Outline each Plasmodium ovale-infected red blood cell.
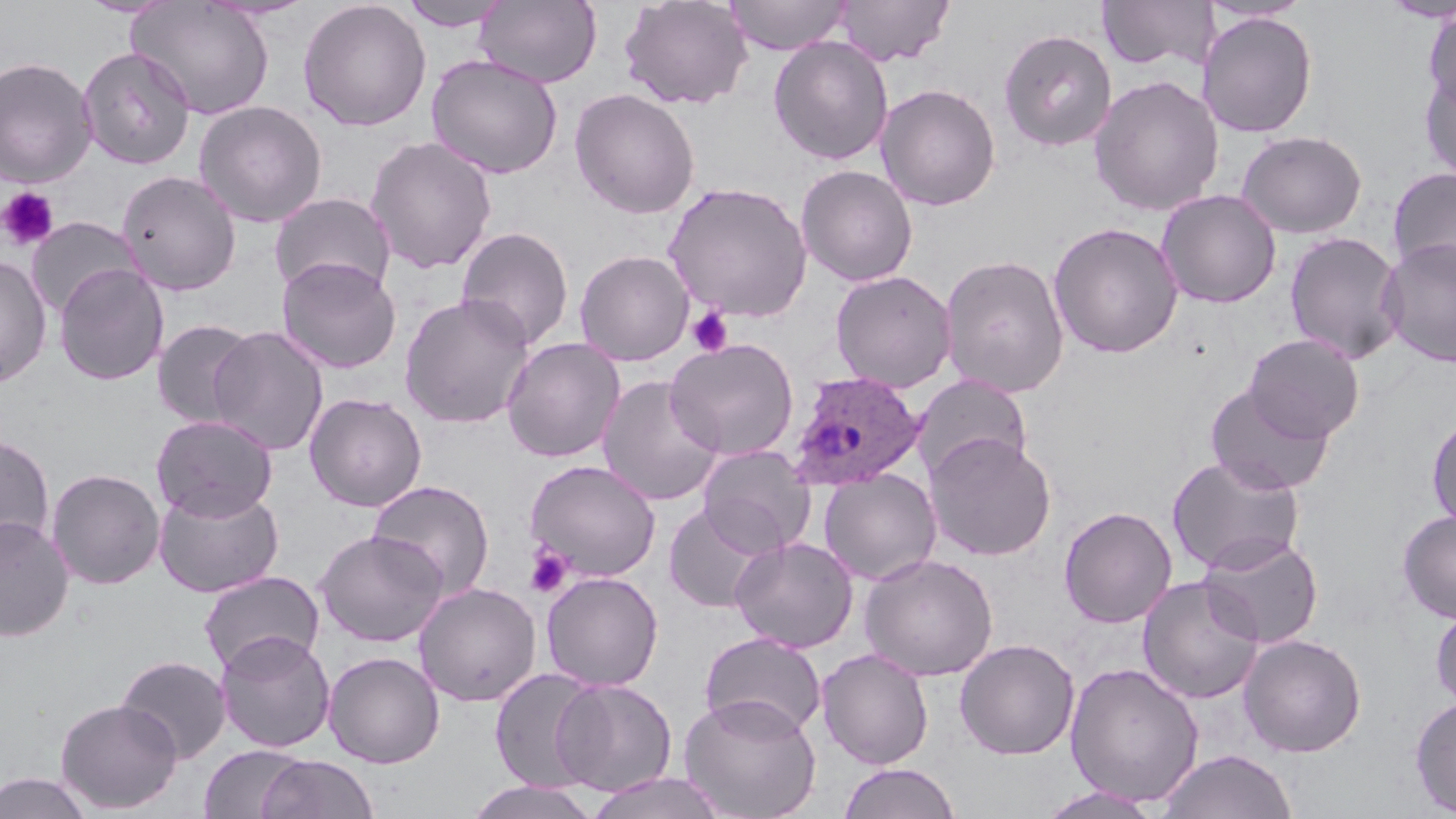

Approximate bounding boxes as (x1, y1, x2, y2) in pixels.
Plasmodium ovale-infected red blood cells: (787, 370, 926, 492).

Summary:
  - Uninfected red blood cell locations: (397, 0, 513, 32), (475, 0, 602, 88), (619, 0, 753, 111), (724, 0, 853, 55), (835, 0, 954, 66), (1380, 0, 1455, 22), (128, 1, 275, 120), (297, 1, 432, 132), (1097, 1, 1217, 74), (1200, 1, 1312, 24), (1422, 7, 1456, 115), (1197, 11, 1318, 138), (998, 28, 1118, 152), (768, 36, 893, 165), (77, 46, 196, 170), (426, 54, 563, 179), (0, 56, 98, 188), (1419, 65, 1456, 186), (1089, 74, 1225, 216), (875, 83, 1001, 211), (569, 88, 701, 219), (193, 100, 328, 228), (1236, 130, 1367, 238), (365, 136, 498, 275), (796, 164, 919, 287), (1387, 166, 1456, 281), (116, 170, 242, 296), (663, 181, 813, 321), (1157, 189, 1281, 308), (269, 192, 396, 299), (26, 217, 141, 319), (1048, 221, 1184, 358), (456, 226, 574, 351), (1284, 231, 1407, 364), (1378, 237, 1456, 368), (574, 249, 695, 366), (939, 253, 1070, 397), (0, 254, 52, 387), (277, 257, 401, 374), (54, 264, 169, 386), (830, 270, 957, 393), (399, 293, 536, 429), (151, 319, 260, 429), (207, 326, 329, 456), (1244, 334, 1365, 443), (501, 337, 625, 463), (664, 337, 800, 460), (912, 373, 1033, 482), (597, 374, 725, 507), (1204, 383, 1335, 496), (304, 392, 427, 512), (150, 414, 278, 521), (1426, 414, 1456, 532), (924, 432, 1056, 562), (0, 434, 55, 558), (697, 445, 816, 557), (1167, 453, 1306, 575), (524, 459, 662, 582), (46, 468, 166, 589), (818, 469, 941, 585), (366, 480, 496, 601), (153, 484, 284, 598), (663, 502, 776, 613), (1058, 506, 1177, 628), (1397, 510, 1456, 623), (0, 514, 75, 641), (314, 530, 449, 647), (1197, 532, 1324, 649), (729, 536, 859, 654), (859, 553, 998, 681), (198, 570, 325, 677), (540, 571, 664, 691), (1137, 575, 1265, 704), (414, 582, 541, 706), (1430, 602, 1456, 711), (214, 631, 336, 753), (698, 631, 826, 739), (1239, 633, 1367, 757), (954, 638, 1080, 760), (817, 648, 934, 769), (323, 651, 445, 768), (115, 655, 232, 764), (1064, 662, 1204, 807), (489, 669, 607, 792), (552, 678, 678, 796), (679, 694, 821, 818), (1409, 695, 1456, 816), (55, 698, 182, 813), (199, 745, 308, 818), (1157, 749, 1298, 819), (257, 754, 379, 818), (837, 762, 962, 819), (0, 771, 94, 819), (586, 771, 727, 819), (464, 781, 605, 819), (1037, 785, 1165, 819)
  - Platelet locations: (0, 187, 59, 250), (686, 307, 733, 357), (524, 544, 574, 598)
  - Slide-level diagnosis: Plasmodium ovale
  - Stain: May-Grünwald-Giemsa
  - Field of view: one of a larger specimen
  - Modality: light microscopy
  - Image size: 1456×819 pixels
  - Magnification: 1000x
  - Preparation: thin blood film